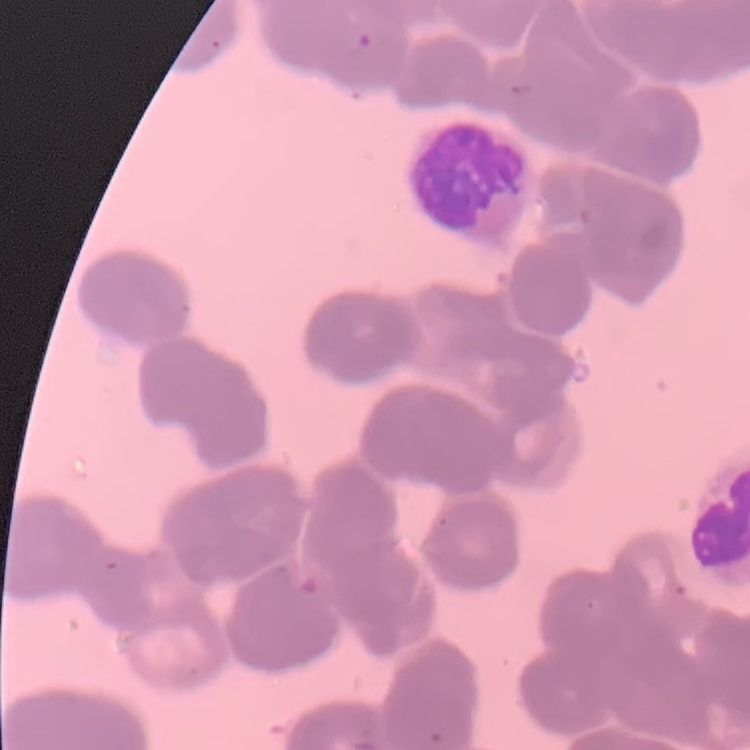 The erythrocytes show rouleaux formation. Thin peripheral smear. Stained with either Field's or Giemsa. Square crop of a larger photomicrograph.